Classify this cell by malaria status.
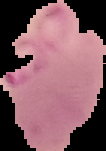
Parasitized.

Summary:
  - Preparation: thin blood smear
  - Image size: 106×151 pixels
  - Image type: cell region segmented out of the field of view; surrounding area masked to black